Locate every Plasmodium vivax-infected red blood cell.
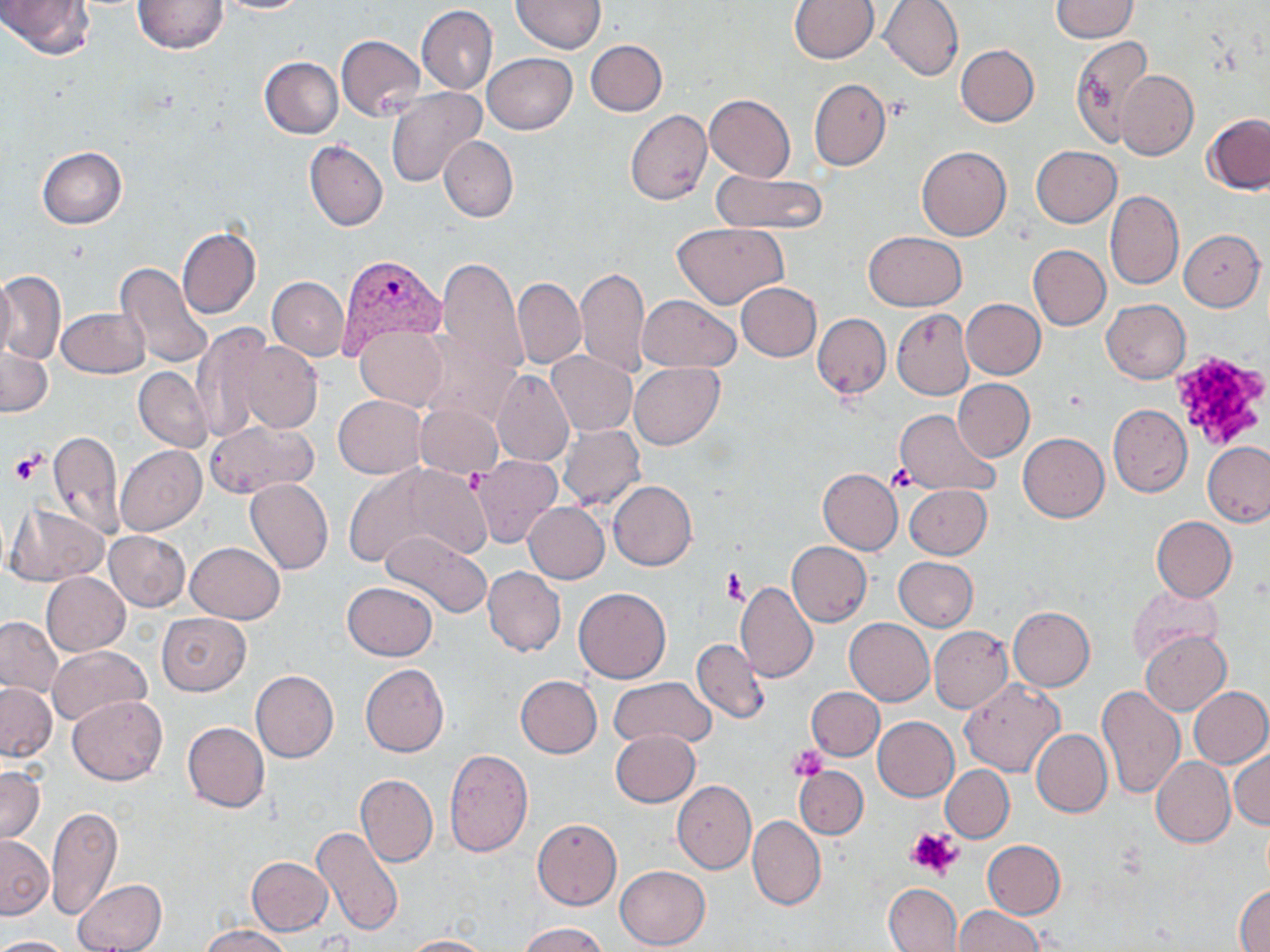

Approximate bounding boxes as named x1/y1/x2/y2 corners in pixels.
Plasmodium vivax-infected red blood cells: (x1=338, y1=253, x2=447, y2=358).

{
  "slide_level_diagnosis": "Plasmodium vivax",
  "magnification": "1000x",
  "modality": "optical microscopy",
  "preparation": "thin blood smear",
  "uninfected_red_blood_cell_locations": "approximate bounding boxes as named x1/y1/x2/y2 corners in pixels: (x1=1, y1=0, x2=95, y2=60), (x1=133, y1=0, x2=227, y2=53), (x1=214, y1=0, x2=308, y2=13), (x1=512, y1=0, x2=605, y2=53), (x1=880, y1=0, x2=965, y2=81), (x1=1050, y1=0, x2=1138, y2=43), (x1=789, y1=1, x2=879, y2=63), (x1=417, y1=5, x2=497, y2=94), (x1=336, y1=34, x2=424, y2=121), (x1=1071, y1=35, x2=1151, y2=147), (x1=585, y1=39, x2=666, y2=116), (x1=956, y1=45, x2=1038, y2=126), (x1=483, y1=53, x2=576, y2=134), (x1=259, y1=56, x2=344, y2=137), (x1=1115, y1=68, x2=1197, y2=161), (x1=809, y1=78, x2=890, y2=171), (x1=386, y1=87, x2=486, y2=188), (x1=705, y1=94, x2=795, y2=182), (x1=625, y1=110, x2=712, y2=204), (x1=1203, y1=113, x2=1270, y2=194), (x1=439, y1=136, x2=517, y2=222), (x1=304, y1=141, x2=387, y2=231), (x1=916, y1=146, x2=1011, y2=241), (x1=1030, y1=146, x2=1121, y2=227), (x1=38, y1=147, x2=127, y2=229), (x1=712, y1=171, x2=829, y2=234), (x1=1105, y1=191, x2=1183, y2=290), (x1=672, y1=223, x2=789, y2=310), (x1=177, y1=227, x2=260, y2=320), (x1=1179, y1=229, x2=1265, y2=311), (x1=863, y1=232, x2=967, y2=311), (x1=1028, y1=244, x2=1111, y2=330), (x1=437, y1=257, x2=529, y2=377), (x1=117, y1=263, x2=216, y2=371), (x1=577, y1=268, x2=650, y2=376), (x1=1, y1=272, x2=65, y2=364), (x1=0, y1=275, x2=17, y2=359), (x1=267, y1=277, x2=349, y2=360), (x1=512, y1=277, x2=586, y2=368), (x1=736, y1=282, x2=821, y2=361), (x1=637, y1=294, x2=741, y2=373), (x1=962, y1=299, x2=1045, y2=379), (x1=1101, y1=299, x2=1191, y2=383), (x1=57, y1=307, x2=149, y2=377), (x1=892, y1=308, x2=973, y2=399), (x1=813, y1=313, x2=891, y2=399), (x1=192, y1=324, x2=274, y2=442), (x1=355, y1=324, x2=447, y2=411), (x1=416, y1=329, x2=520, y2=427), (x1=232, y1=339, x2=322, y2=434), (x1=1, y1=348, x2=52, y2=416), (x1=547, y1=351, x2=636, y2=436), (x1=630, y1=363, x2=723, y2=449), (x1=134, y1=367, x2=213, y2=452), (x1=490, y1=370, x2=575, y2=467), (x1=953, y1=378, x2=1034, y2=461), (x1=333, y1=395, x2=427, y2=479), (x1=415, y1=403, x2=504, y2=478), (x1=1107, y1=403, x2=1192, y2=497), (x1=894, y1=409, x2=999, y2=496), (x1=205, y1=419, x2=319, y2=497), (x1=558, y1=423, x2=645, y2=512), (x1=48, y1=429, x2=124, y2=536), (x1=1018, y1=432, x2=1109, y2=522), (x1=1203, y1=442, x2=1270, y2=527), (x1=117, y1=445, x2=205, y2=535), (x1=472, y1=455, x2=561, y2=547), (x1=346, y1=463, x2=488, y2=570), (x1=818, y1=468, x2=903, y2=556), (x1=244, y1=479, x2=333, y2=575), (x1=608, y1=480, x2=696, y2=570), (x1=904, y1=484, x2=991, y2=559), (x1=524, y1=502, x2=609, y2=583), (x1=7, y1=504, x2=109, y2=585), (x1=1151, y1=516, x2=1237, y2=603), (x1=104, y1=530, x2=190, y2=611), (x1=380, y1=531, x2=493, y2=618), (x1=185, y1=542, x2=284, y2=623), (x1=787, y1=542, x2=872, y2=626), (x1=894, y1=557, x2=978, y2=632), (x1=483, y1=566, x2=566, y2=656), (x1=41, y1=572, x2=129, y2=656), (x1=342, y1=582, x2=437, y2=661), (x1=734, y1=582, x2=818, y2=683), (x1=1127, y1=586, x2=1224, y2=663), (x1=573, y1=588, x2=671, y2=683), (x1=1008, y1=606, x2=1095, y2=689), (x1=157, y1=612, x2=250, y2=695), (x1=0, y1=616, x2=62, y2=698), (x1=845, y1=618, x2=935, y2=705), (x1=930, y1=626, x2=1012, y2=713), (x1=1141, y1=631, x2=1230, y2=715), (x1=693, y1=639, x2=767, y2=723), (x1=48, y1=645, x2=151, y2=725), (x1=360, y1=664, x2=449, y2=757), (x1=250, y1=671, x2=338, y2=763), (x1=515, y1=675, x2=602, y2=758), (x1=609, y1=677, x2=716, y2=750), (x1=959, y1=679, x2=1065, y2=776), (x1=0, y1=683, x2=55, y2=761), (x1=806, y1=686, x2=885, y2=760), (x1=1096, y1=686, x2=1185, y2=798), (x1=1187, y1=686, x2=1270, y2=767), (x1=67, y1=694, x2=168, y2=785), (x1=873, y1=716, x2=958, y2=801), (x1=182, y1=721, x2=270, y2=812), (x1=610, y1=729, x2=700, y2=807), (x1=1031, y1=729, x2=1112, y2=818), (x1=1230, y1=745, x2=1269, y2=831), (x1=443, y1=748, x2=533, y2=857), (x1=1152, y1=756, x2=1235, y2=848), (x1=941, y1=765, x2=1014, y2=842), (x1=0, y1=766, x2=45, y2=844), (x1=794, y1=767, x2=867, y2=839), (x1=355, y1=773, x2=438, y2=867), (x1=672, y1=780, x2=756, y2=873), (x1=47, y1=805, x2=122, y2=919), (x1=748, y1=815, x2=826, y2=910), (x1=532, y1=817, x2=622, y2=910), (x1=311, y1=827, x2=403, y2=935), (x1=0, y1=834, x2=53, y2=920), (x1=981, y1=839, x2=1066, y2=918), (x1=246, y1=857, x2=333, y2=935), (x1=615, y1=866, x2=710, y2=950), (x1=73, y1=879, x2=167, y2=951), (x1=883, y1=883, x2=962, y2=951), (x1=1235, y1=883, x2=1270, y2=950), (x1=953, y1=906, x2=1045, y2=952), (x1=519, y1=922, x2=610, y2=952), (x1=201, y1=925, x2=295, y2=952), (x1=0, y1=935, x2=76, y2=951), (x1=402, y1=935, x2=495, y2=952)",
  "image_size": "1270×952 pixels",
  "platelet_locations": "approximate bounding boxes as named x1/y1/x2/y2 corners in pixels: (x1=1169, y1=352, x2=1269, y2=452), (x1=9, y1=451, x2=45, y2=484), (x1=888, y1=464, x2=917, y2=492), (x1=462, y1=466, x2=483, y2=496), (x1=721, y1=568, x2=747, y2=605), (x1=789, y1=745, x2=827, y2=780), (x1=907, y1=826, x2=961, y2=879)",
  "field_of_view": "one of a larger specimen",
  "stain": "May-Grünwald-Giemsa"
}